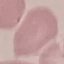

result = negative for malaria parasites
capture = smartphone camera at the microscope eyepiece
stain = Giemsa
image type = automatically extracted cell patch, resized to 64 × 64 pixels
preparation = thin blood film